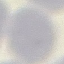
Malaria status: uninfected. Thin smear of blood. Giemsa stain. Automatically extracted cell patch, resized to 64 × 64 pixels. Acquired by smartphone through the microscope eyepiece.